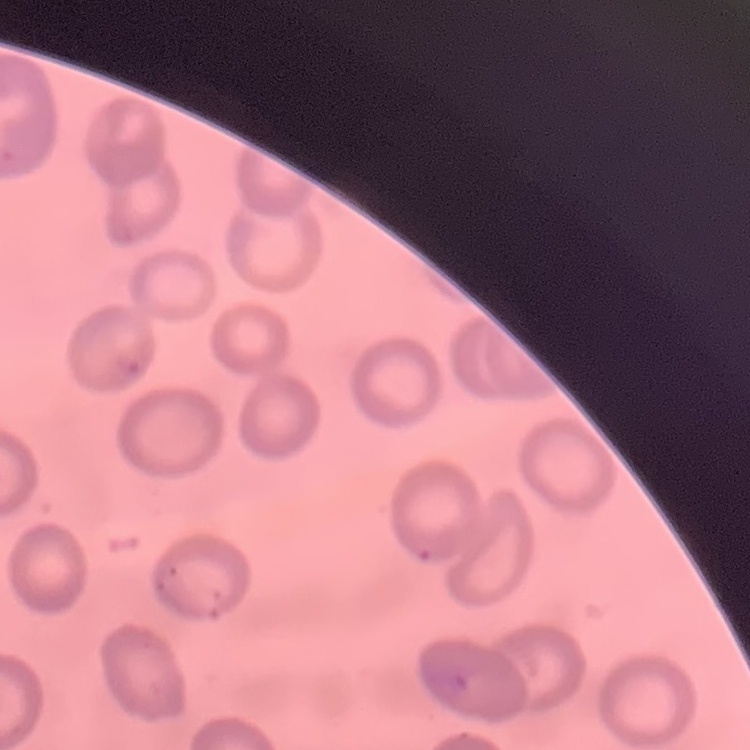
{
  "erythrocyte_morphology": "no rouleaux formation",
  "image_type": "square crop of a larger photomicrograph",
  "stain": "Field's or Giemsa",
  "preparation": "thin blood smear"
}